Report the malaria status of this cell.
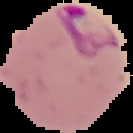
Parasitized.

The area outside the segmented cell region is set to black. From a thin blood film. Image is 133×133 pixels.